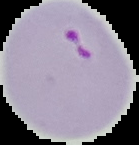 The area outside the segmented cell region is set to black. Malaria status: parasitized. From a thin blood film. Image is 139×145 pixels.